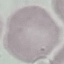

Summary:
  - Malaria status: uninfected
  - Capture: smartphone camera at the microscope eyepiece
  - Image type: automatically extracted cell patch, resized to 64 × 64 pixels
  - Preparation: thin blood smear
  - Stain: Giemsa